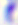

Summary:
  - Identification: Toxoplasma gondii
  - Magnification: 400x
  - Modality: micrograph